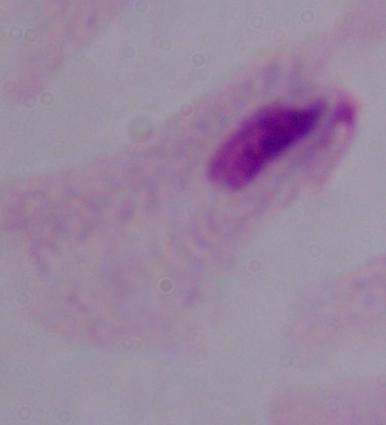

1000x magnification. A trichomonad is seen. Micrograph.